Point out Plasmodium parasites and leukocytes.
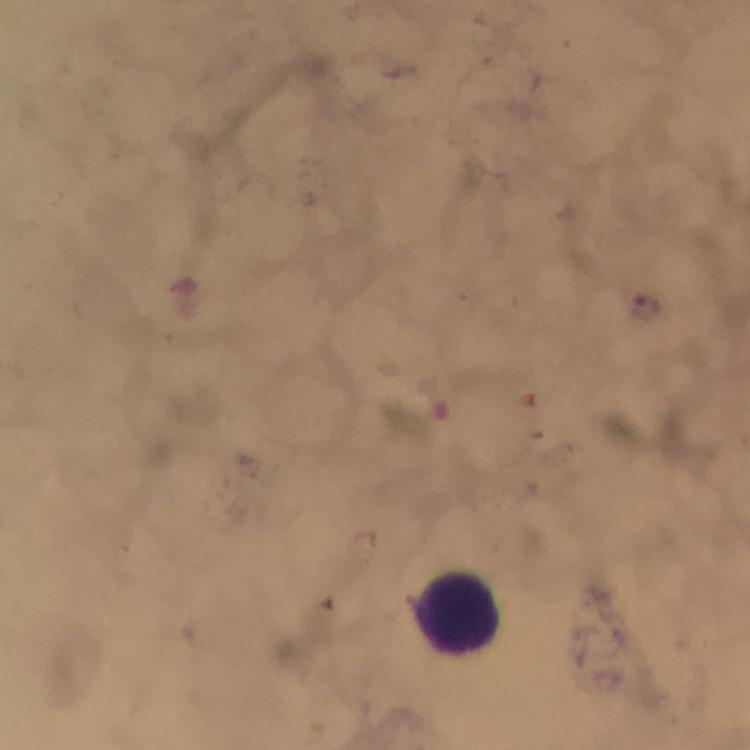
Approximate object centers, in pixels from the top-left corner.
Plasmodium parasites: (x=646, y=308).
Leukocytes: (x=461, y=614).

Image is 750×750 pixels. At 100x magnification. A crop from one field of view. Photographed with a smartphone mounted on the microscope. From a malaria diagnostic workup. Immersion oil applied. Giemsa-stained preparation. Thick smear.